Name the cell type shown.
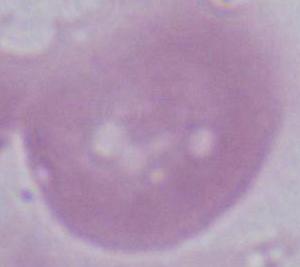

This is an erythrocyte.

Summary:
  - Modality: micrograph
  - Magnification: 1000x